Classify this cell by malaria status.
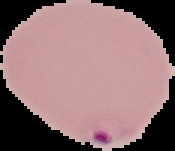

Parasitized.

Image is 175×151 pixels. From a thin blood smear. Segmented cell region on a black background.